Give the position of every malaria parasite.
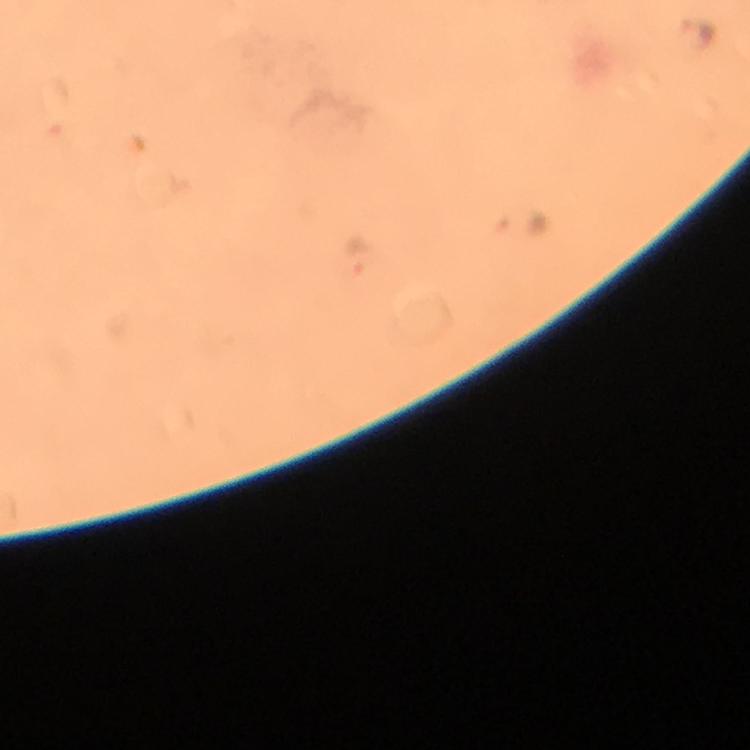
Approximate centers as (x, y) in pixels.
Malaria parasites: (699, 31), (360, 257).

Thick blood smear. Cropped region of a single field of view. Photographed with a smartphone mounted on the microscope. From a malaria diagnostic workup. Immersion oil was used. At 100x magnification. Image is 750×750 pixels. Giemsa stain.